Assess this cell for malaria.
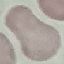

It is uninfected.

Acquired by smartphone through the microscope eyepiece. Giemsa-stained preparation. Automatically extracted cell patch, resized to 64 × 64 pixels. Thin smear of blood.